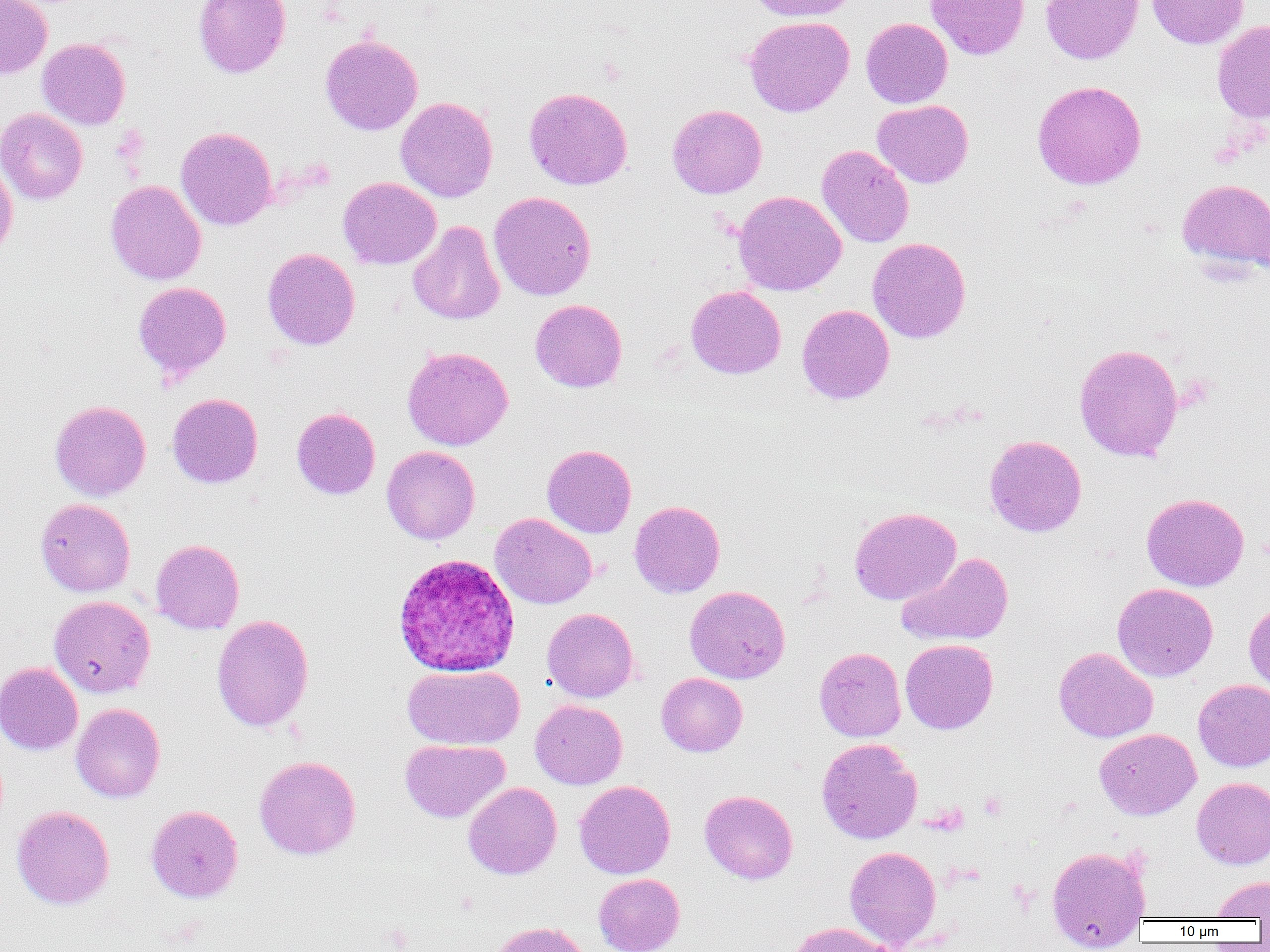 Approximate bounding boxes as [x1, y1, x2, y2] in pixels. Platelet locations: [978, 792, 1007, 820]. Uninfected red blood cell locations: [0, 0, 52, 79], [193, 0, 291, 78], [747, 0, 857, 22], [925, 0, 1030, 60], [1040, 0, 1143, 64], [1146, 0, 1249, 49], [744, 16, 855, 117], [861, 17, 953, 108], [1212, 19, 1270, 124], [320, 34, 423, 135], [37, 38, 131, 130], [1032, 80, 1147, 190], [524, 87, 633, 190], [395, 96, 498, 202], [872, 99, 974, 188], [667, 104, 767, 199], [0, 108, 88, 205], [175, 126, 277, 230], [816, 145, 915, 248], [0, 157, 18, 259], [338, 177, 441, 269], [1177, 179, 1270, 273], [105, 180, 206, 285], [489, 191, 596, 301], [734, 191, 846, 296], [408, 220, 505, 325], [867, 237, 971, 343], [262, 248, 360, 350], [133, 281, 231, 382], [686, 285, 786, 379], [530, 299, 627, 392], [796, 304, 894, 404], [1073, 343, 1184, 462], [402, 346, 513, 451], [167, 393, 263, 488], [50, 400, 151, 501], [291, 407, 380, 500], [984, 435, 1087, 537], [542, 444, 636, 538], [381, 445, 480, 544], [1141, 493, 1249, 591], [36, 498, 136, 596], [629, 500, 725, 598], [849, 507, 962, 605], [489, 513, 597, 609], [151, 539, 245, 634], [896, 552, 1014, 647], [1112, 583, 1218, 682], [685, 586, 790, 683], [49, 595, 156, 697], [1244, 601, 1270, 695], [542, 608, 639, 702], [211, 614, 314, 732], [900, 639, 998, 734], [814, 647, 906, 742], [1053, 647, 1158, 743], [0, 661, 83, 755], [403, 665, 524, 750], [656, 673, 747, 757], [1193, 679, 1270, 771], [529, 700, 627, 789], [70, 703, 165, 802], [1094, 728, 1201, 820], [816, 738, 922, 844], [400, 739, 510, 823], [254, 756, 361, 860], [1191, 777, 1270, 869], [574, 780, 675, 879], [463, 782, 562, 880], [700, 790, 798, 884], [12, 805, 115, 909], [146, 805, 243, 903], [844, 846, 942, 948], [1046, 846, 1151, 950], [593, 873, 685, 952], [1211, 874, 1270, 920], [491, 921, 589, 952], [785, 922, 897, 952]. Plasmodium ovale-infected red blood cell locations: [392, 553, 520, 676]. Slide-level diagnosis: Plasmodium ovale. Image is 1270×952 pixels. Thin blood smear. Captured at 1000x magnification. Single field of view. Optical microscopy.